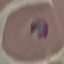
result = malaria parasites identified
image type = automatically extracted cell patch, resized to 64 × 64 pixels
stain = Giemsa
preparation = thin blood film
capture = smartphone through the microscope eyepiece